Point out each leukocyte.
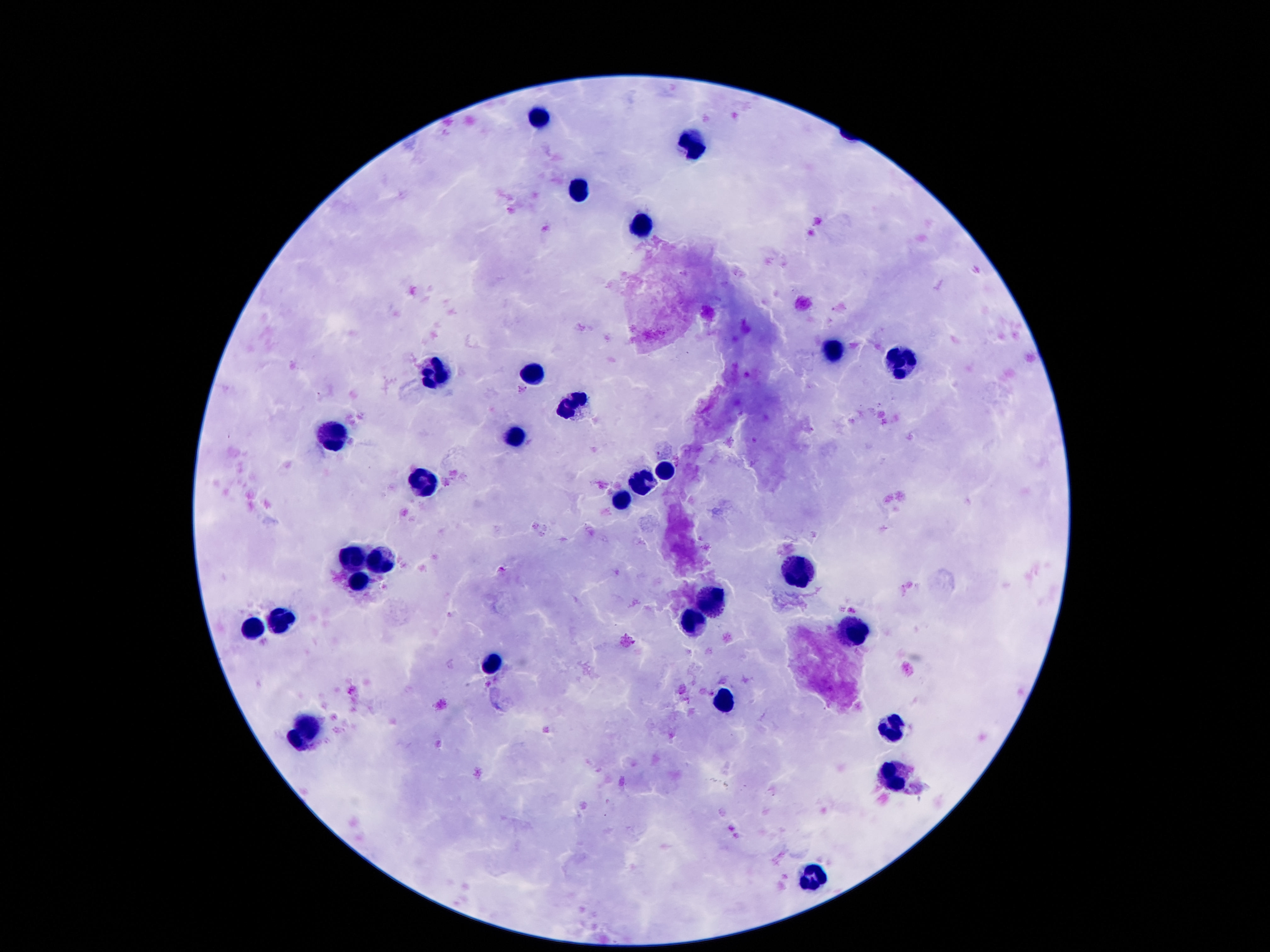
Approximate centers as (x, y) in pixels.
Leukocytes: (539, 115), (692, 143), (576, 192), (643, 223), (830, 352), (905, 365), (530, 371), (435, 376), (574, 406), (334, 438), (515, 439), (663, 470), (641, 483), (425, 484), (623, 502), (357, 559), (383, 560), (798, 574), (359, 582), (714, 599), (688, 620), (283, 621), (251, 631), (851, 634), (492, 666), (725, 700), (310, 724), (892, 728), (295, 742), (893, 780), (814, 877).

capture = smartphone camera through the microscope eyepiece
stain = Giemsa
magnification = 100x
image size = 1270×952 pixels
field of view = single
preparation = thick peripheral-blood smear
patient malaria status = negative